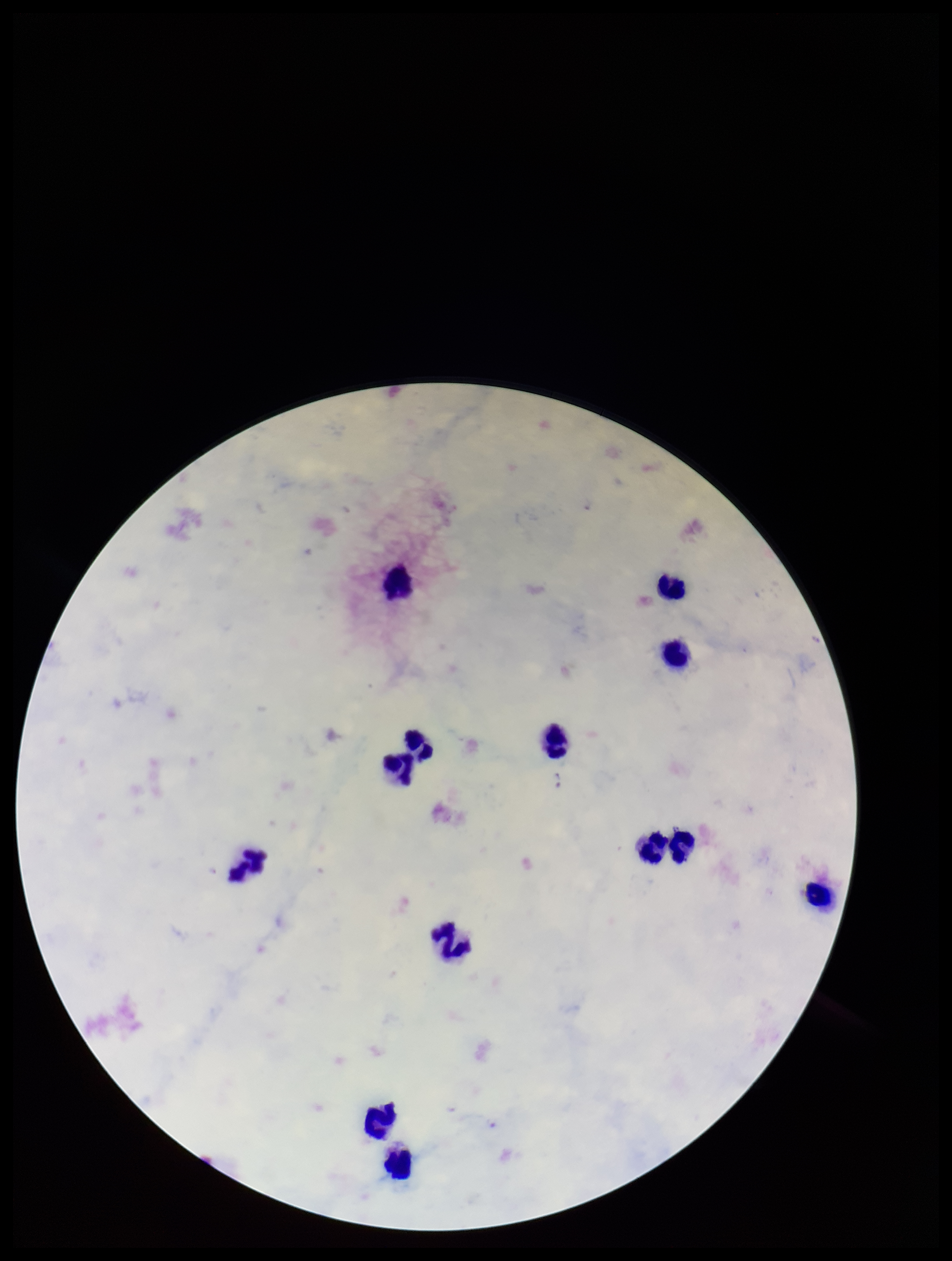
image size = 952×1261 pixels
patient malaria status = infected
leukocyte count = 13
field of view = one from this slide
preparation = thick smear
capture = smartphone photograph through the microscope eyepiece
species reported for this patient = Plasmodium falciparum
Plasmodium parasites = none identified
stain = Giemsa
parasite count = 0